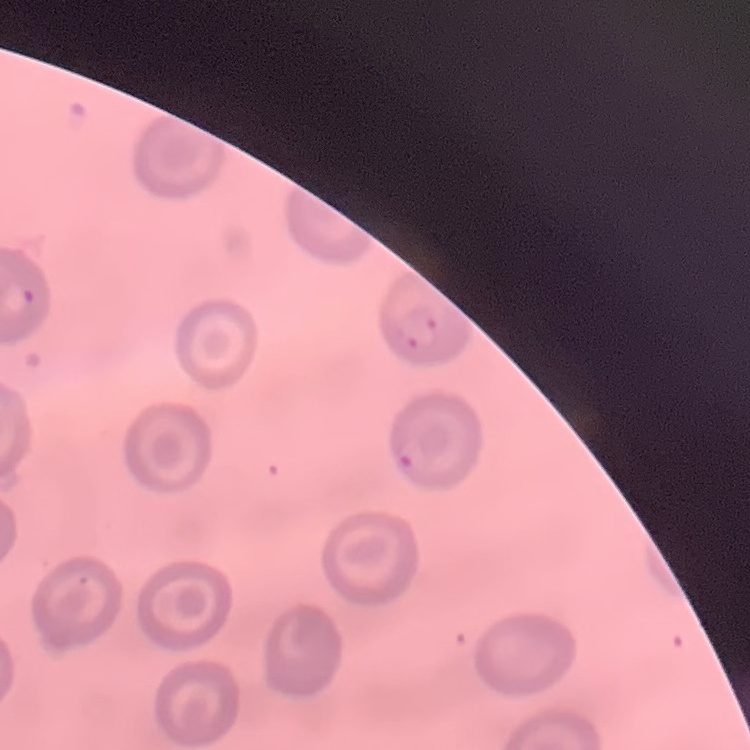
erythrocyte morphology = no rouleaux formation
stain = Field's or Giemsa
image type = square crop of a larger photomicrograph
preparation = thin peripheral smear